Look for Plasmodium parasites.
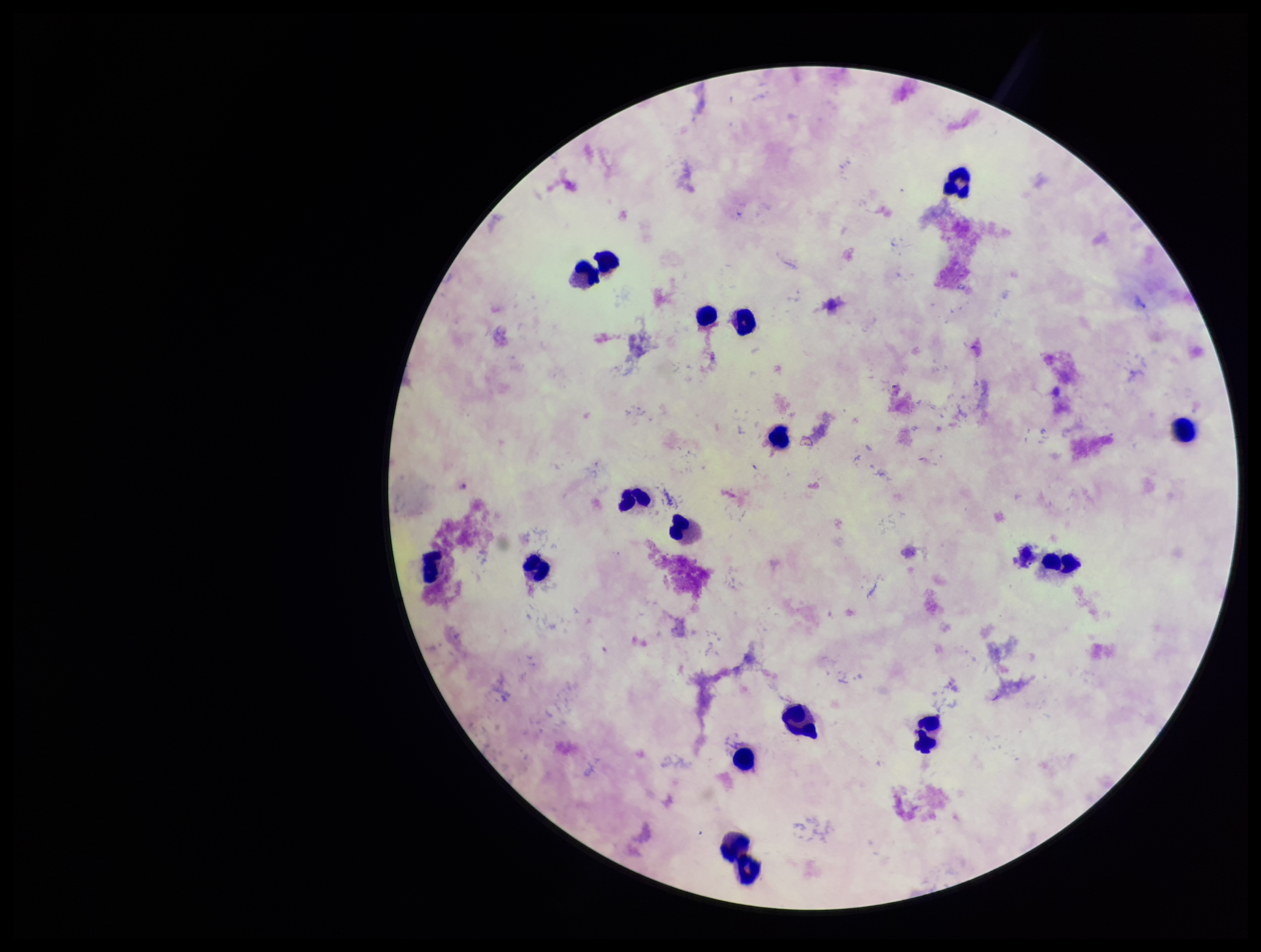
None seen.

Summary:
  - Capture: smartphone photograph through the microscope eyepiece
  - Patient malaria status: infected
  - Image size: 1261×952 pixels
  - Stain: Giemsa
  - Parasite count: 0
  - Field of view: one from this slide
  - Species reported for this patient: Plasmodium falciparum
  - Preparation: thick smear
  - Leukocyte count: 17